Locate every Plasmodium parasite.
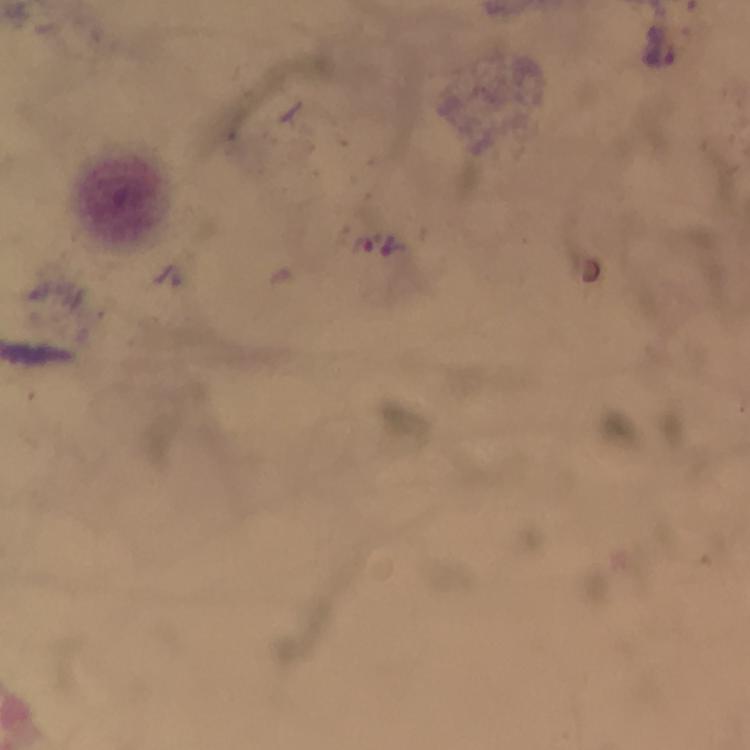
Approximate centers as {x, y} in pixels.
Plasmodium parasites: {660, 45}.

Summary:
  - Preparation: thick blood film
  - Magnification: 100x
  - Cropped from: a single field of view
  - Stain: Giemsa
  - Capture: smartphone camera through the microscope
  - Image size: 750×750 pixels
  - Context: from a malaria diagnostic workup
  - Immersion oil: used